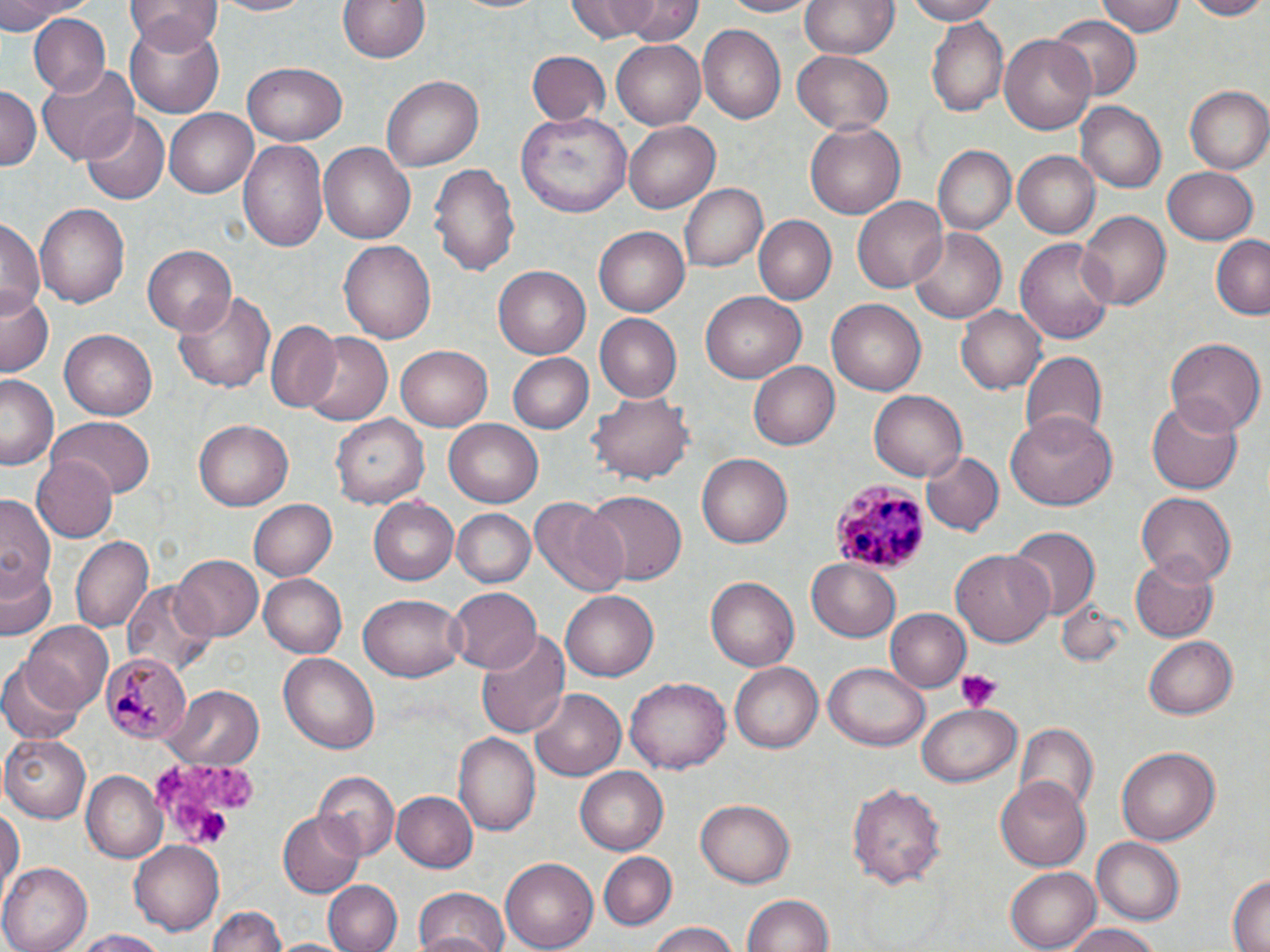

Approximate bounding boxes as named x1/y1/x2/y2 corners in pixels. Uninfected red blood cell locations: (x1=0, y1=0, x2=91, y2=30), (x1=126, y1=0, x2=221, y2=54), (x1=210, y1=0, x2=316, y2=17), (x1=336, y1=0, x2=433, y2=64), (x1=445, y1=0, x2=554, y2=15), (x1=567, y1=0, x2=661, y2=43), (x1=616, y1=0, x2=703, y2=46), (x1=715, y1=0, x2=823, y2=17), (x1=801, y1=0, x2=899, y2=57), (x1=903, y1=0, x2=1001, y2=24), (x1=1095, y1=0, x2=1184, y2=37), (x1=1181, y1=0, x2=1270, y2=20), (x1=1048, y1=12, x2=1138, y2=100), (x1=27, y1=14, x2=111, y2=100), (x1=927, y1=17, x2=1007, y2=115), (x1=124, y1=21, x2=224, y2=118), (x1=696, y1=23, x2=786, y2=125), (x1=1000, y1=32, x2=1100, y2=135), (x1=612, y1=38, x2=705, y2=128), (x1=527, y1=50, x2=609, y2=125), (x1=793, y1=51, x2=895, y2=135), (x1=242, y1=64, x2=344, y2=146), (x1=38, y1=65, x2=139, y2=163), (x1=382, y1=75, x2=484, y2=172), (x1=0, y1=86, x2=41, y2=171), (x1=1185, y1=86, x2=1270, y2=172), (x1=1075, y1=102, x2=1165, y2=193), (x1=165, y1=108, x2=257, y2=198), (x1=80, y1=111, x2=169, y2=202), (x1=520, y1=111, x2=631, y2=217), (x1=803, y1=121, x2=908, y2=221), (x1=625, y1=122, x2=719, y2=213), (x1=239, y1=137, x2=329, y2=251), (x1=320, y1=144, x2=416, y2=243), (x1=933, y1=145, x2=1015, y2=234), (x1=1014, y1=151, x2=1100, y2=238), (x1=428, y1=162, x2=521, y2=277), (x1=1161, y1=167, x2=1259, y2=244), (x1=679, y1=183, x2=768, y2=273), (x1=853, y1=196, x2=947, y2=293), (x1=35, y1=203, x2=129, y2=309), (x1=1075, y1=210, x2=1171, y2=312), (x1=755, y1=215, x2=837, y2=305), (x1=0, y1=216, x2=43, y2=320), (x1=594, y1=225, x2=690, y2=315), (x1=910, y1=227, x2=1009, y2=323), (x1=1211, y1=234, x2=1270, y2=320), (x1=339, y1=238, x2=437, y2=346), (x1=1016, y1=238, x2=1115, y2=345), (x1=142, y1=243, x2=236, y2=334), (x1=494, y1=266, x2=591, y2=359), (x1=2, y1=288, x2=54, y2=378), (x1=173, y1=289, x2=277, y2=395), (x1=701, y1=291, x2=807, y2=384), (x1=826, y1=299, x2=927, y2=396), (x1=957, y1=305, x2=1047, y2=395), (x1=595, y1=314, x2=683, y2=402), (x1=265, y1=322, x2=343, y2=411), (x1=61, y1=329, x2=158, y2=419), (x1=297, y1=331, x2=395, y2=427), (x1=1166, y1=337, x2=1264, y2=441), (x1=396, y1=344, x2=497, y2=431), (x1=1018, y1=350, x2=1107, y2=444), (x1=506, y1=352, x2=592, y2=435), (x1=750, y1=359, x2=844, y2=450), (x1=1, y1=374, x2=61, y2=472), (x1=592, y1=389, x2=692, y2=485), (x1=868, y1=389, x2=967, y2=481), (x1=1146, y1=398, x2=1244, y2=495), (x1=1006, y1=412, x2=1119, y2=510), (x1=330, y1=413, x2=430, y2=509), (x1=49, y1=418, x2=154, y2=499), (x1=195, y1=418, x2=294, y2=511), (x1=445, y1=420, x2=544, y2=507), (x1=921, y1=450, x2=1002, y2=535), (x1=698, y1=453, x2=793, y2=549), (x1=30, y1=454, x2=116, y2=543), (x1=581, y1=490, x2=687, y2=585), (x1=1136, y1=492, x2=1237, y2=587), (x1=1, y1=495, x2=57, y2=594), (x1=369, y1=496, x2=460, y2=587), (x1=531, y1=497, x2=629, y2=599), (x1=249, y1=498, x2=337, y2=580), (x1=454, y1=509, x2=535, y2=587), (x1=1008, y1=526, x2=1100, y2=619), (x1=71, y1=535, x2=154, y2=632), (x1=953, y1=547, x2=1055, y2=647), (x1=169, y1=554, x2=262, y2=642), (x1=1129, y1=557, x2=1221, y2=643), (x1=806, y1=559, x2=901, y2=641), (x1=2, y1=563, x2=59, y2=642), (x1=260, y1=573, x2=348, y2=656), (x1=706, y1=577, x2=800, y2=671), (x1=123, y1=579, x2=217, y2=679), (x1=444, y1=585, x2=545, y2=674), (x1=561, y1=591, x2=660, y2=683), (x1=357, y1=593, x2=465, y2=683), (x1=884, y1=608, x2=971, y2=693), (x1=20, y1=622, x2=115, y2=714), (x1=475, y1=629, x2=569, y2=739), (x1=1144, y1=635, x2=1239, y2=720), (x1=278, y1=652, x2=381, y2=754), (x1=826, y1=661, x2=930, y2=751), (x1=731, y1=662, x2=823, y2=753), (x1=1, y1=664, x2=85, y2=744), (x1=624, y1=677, x2=730, y2=777), (x1=167, y1=686, x2=263, y2=769), (x1=529, y1=689, x2=626, y2=781), (x1=917, y1=706, x2=1021, y2=786), (x1=1015, y1=725, x2=1098, y2=815), (x1=455, y1=734, x2=540, y2=837), (x1=2, y1=735, x2=90, y2=822), (x1=1116, y1=746, x2=1219, y2=844), (x1=576, y1=769, x2=668, y2=854), (x1=82, y1=771, x2=167, y2=861), (x1=312, y1=772, x2=399, y2=861), (x1=994, y1=774, x2=1090, y2=869), (x1=846, y1=778, x2=947, y2=888), (x1=392, y1=790, x2=479, y2=873), (x1=0, y1=800, x2=23, y2=903), (x1=696, y1=800, x2=794, y2=888), (x1=278, y1=810, x2=367, y2=898), (x1=1091, y1=837, x2=1186, y2=923), (x1=129, y1=841, x2=226, y2=937), (x1=598, y1=852, x2=677, y2=929), (x1=498, y1=857, x2=597, y2=952), (x1=3, y1=864, x2=94, y2=952), (x1=1005, y1=865, x2=1102, y2=950), (x1=1226, y1=869, x2=1270, y2=952), (x1=323, y1=878, x2=401, y2=952), (x1=412, y1=886, x2=510, y2=952), (x1=739, y1=892, x2=835, y2=952), (x1=206, y1=904, x2=289, y2=952), (x1=643, y1=924, x2=744, y2=952), (x1=1065, y1=924, x2=1168, y2=952), (x1=66, y1=928, x2=176, y2=950). Platelet locations: (x1=955, y1=669, x2=1001, y2=711), (x1=150, y1=757, x2=259, y2=846). Plasmodium malariae-infected red blood cell locations: (x1=833, y1=478, x2=927, y2=575), (x1=101, y1=653, x2=193, y2=743). Slide-level diagnosis: Plasmodium malariae. Optical microscopy. Captured at 1000x magnification. May-Grünwald-Giemsa-stained preparation. Image is 1270×952 pixels. Single field of view. Thin blood film.